Report the malaria status of this cell.
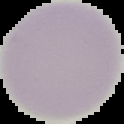

It is uninfected.

image type = cell region segmented out of the field of view; surrounding area masked to black
image size = 124×124 pixels
preparation = thin blood film